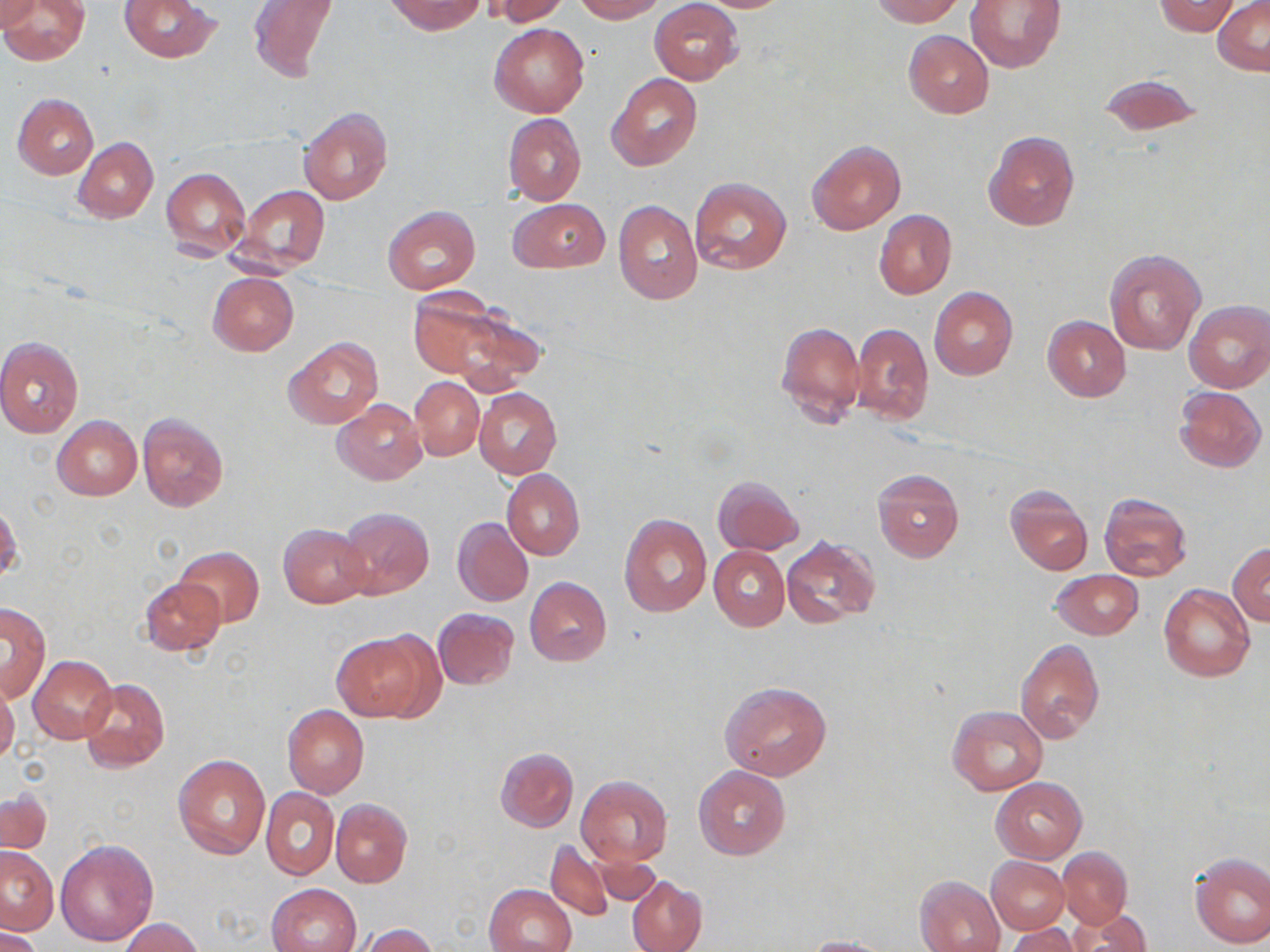
{
  "slide_level_diagnosis": "negative for blood parasites",
  "field_of_view": "one of a larger specimen",
  "modality": "light microscopy",
  "uninfected_red_blood_cell_locations": "approximate bounding boxes as (x1, y1, x2, y2) in pixels: (0, 0, 41, 33), (119, 0, 221, 62), (386, 0, 486, 35), (487, 0, 569, 26), (573, 0, 665, 22), (687, 0, 796, 12), (870, 0, 962, 26), (965, 0, 1067, 73), (1212, 0, 1270, 75), (0, 1, 90, 65), (247, 1, 340, 81), (650, 1, 743, 85), (1152, 1, 1242, 35), (490, 23, 588, 117), (903, 30, 994, 119), (607, 74, 702, 172), (1096, 75, 1202, 138), (11, 92, 98, 179), (297, 107, 392, 206), (503, 113, 585, 206), (982, 131, 1080, 232), (73, 137, 157, 223), (806, 140, 905, 235), (162, 168, 251, 261), (690, 178, 791, 274), (237, 185, 328, 273), (510, 199, 609, 273), (613, 200, 702, 303), (384, 206, 480, 294), (874, 209, 957, 299), (1103, 248, 1206, 356), (208, 272, 299, 356), (930, 286, 1017, 381), (407, 292, 532, 389), (1184, 300, 1270, 393), (1042, 315, 1131, 401), (776, 321, 865, 428), (850, 323, 933, 425), (0, 336, 84, 437), (283, 338, 383, 429), (411, 376, 484, 460), (485, 386, 568, 560), (1175, 387, 1267, 471), (474, 388, 561, 479), (333, 398, 426, 485), (137, 413, 230, 513), (53, 416, 141, 500), (872, 468, 964, 563), (502, 469, 584, 560), (713, 476, 803, 555), (1005, 484, 1093, 574), (1099, 493, 1192, 581), (1, 504, 22, 587), (338, 506, 434, 599), (619, 515, 711, 618), (453, 517, 533, 607), (448, 519, 526, 693), (279, 523, 371, 608), (782, 536, 881, 629), (1230, 541, 1270, 625), (709, 546, 789, 630), (174, 547, 264, 628), (1050, 568, 1143, 638), (140, 577, 225, 655), (525, 577, 611, 666), (1159, 585, 1255, 681), (2, 603, 50, 700), (433, 608, 518, 690), (332, 630, 436, 722), (1015, 638, 1104, 742), (27, 656, 117, 743), (0, 675, 20, 764), (79, 678, 168, 773), (720, 681, 831, 779), (283, 705, 369, 797), (947, 705, 1046, 795), (495, 747, 579, 833), (174, 753, 270, 857), (693, 767, 791, 860), (576, 775, 672, 865), (992, 777, 1087, 862), (260, 787, 338, 881), (2, 790, 52, 855), (330, 799, 412, 888), (54, 838, 158, 947), (545, 839, 613, 921), (1, 846, 57, 936), (1057, 847, 1132, 928), (589, 851, 660, 905), (1190, 853, 1270, 948), (987, 857, 1070, 933), (627, 875, 707, 952), (916, 875, 1005, 952), (266, 882, 361, 952), (484, 883, 576, 952), (1067, 909, 1152, 952), (119, 918, 204, 952), (358, 924, 436, 952), (1, 925, 44, 952), (1004, 925, 1081, 952), (800, 936, 900, 952)",
  "preparation": "thin blood smear",
  "stain": "May-Grünwald-Giemsa",
  "magnification": "1000x",
  "image_size": "1270×952 pixels"
}